Give the position of every Plasmodium parasite visible.
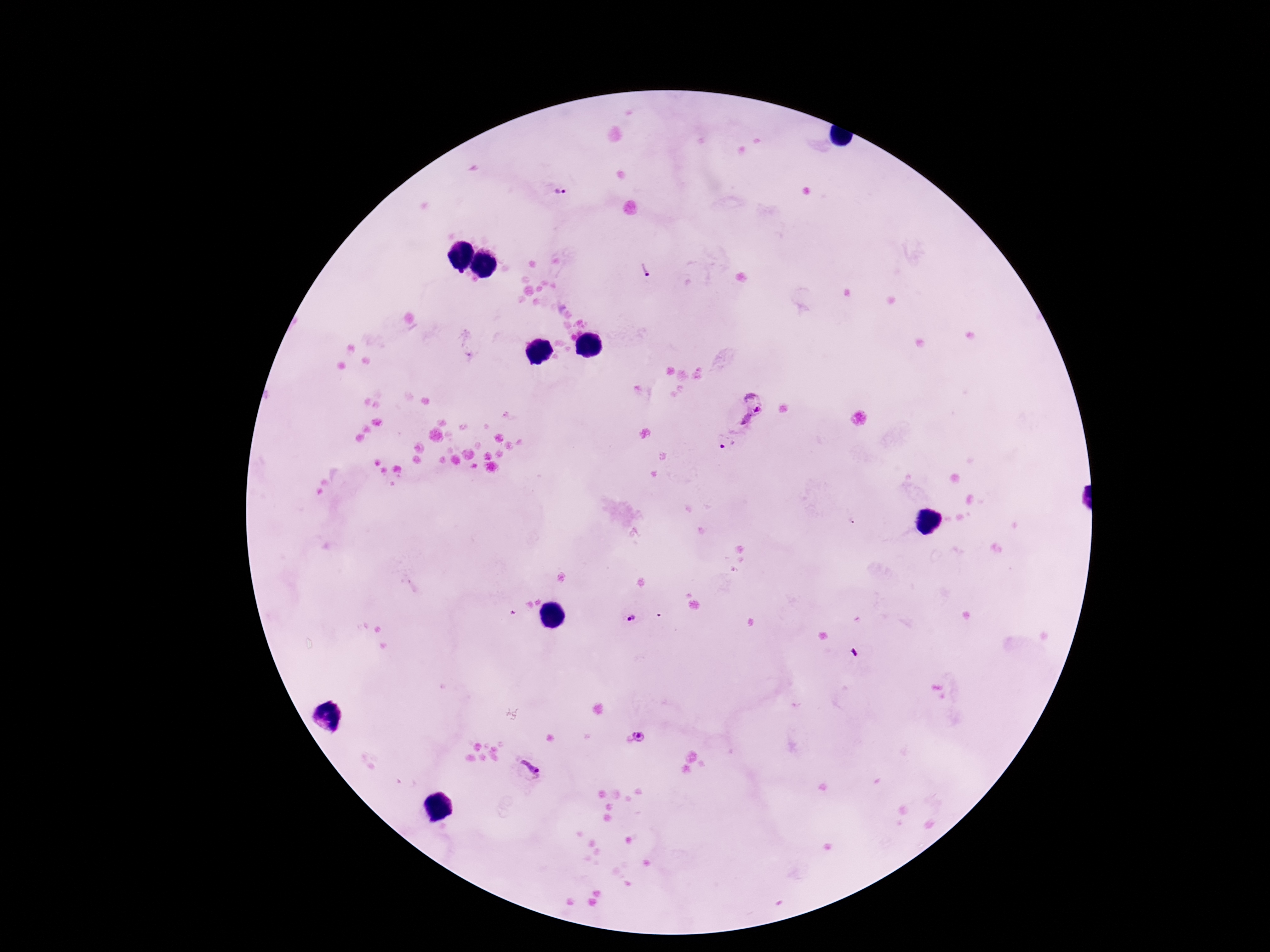

Approximate centers as {x, y} in pixels.
Plasmodium parasites: {561, 190}, {645, 271}, {746, 407}, {727, 441}, {632, 619}, {637, 737}, {530, 768}.

preparation = thick blood film
field of view = single
patient malaria status = infected
magnification = 100x
capture = smartphone camera through the microscope eyepiece
stain = Giemsa
image size = 1270×952 pixels